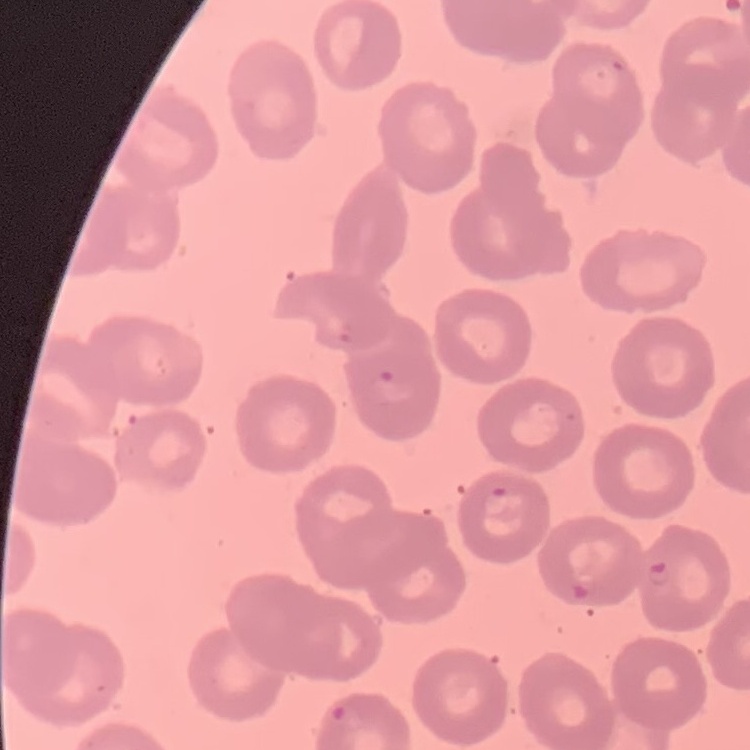
The erythrocytes exhibit no rouleaux formation. Field's or Giemsa stain. One tile cut from a larger photomicrograph. Thin blood smear.